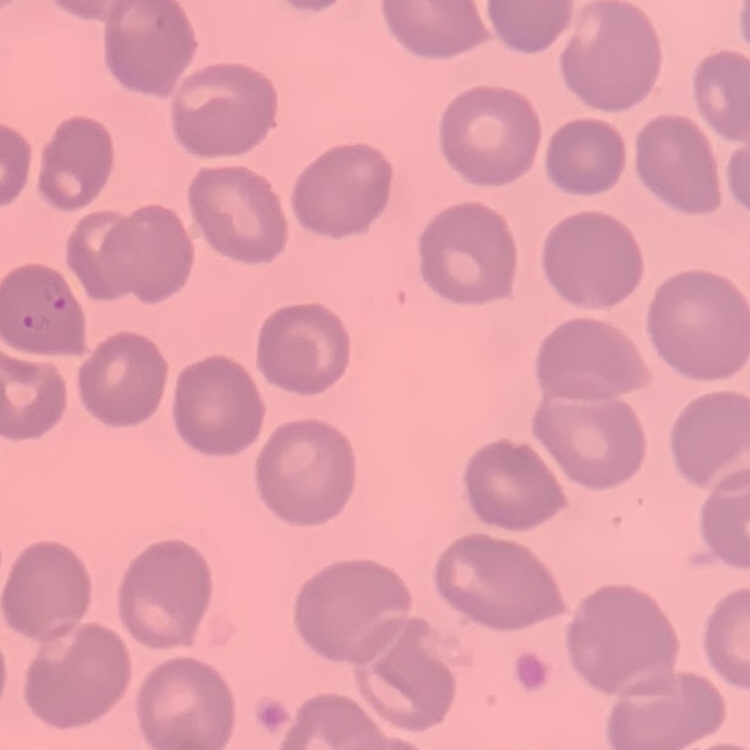

erythrocyte morphology = no rouleaux formation
stain = Field's or Giemsa
image type = square crop of a larger photomicrograph
preparation = thin peripheral smear